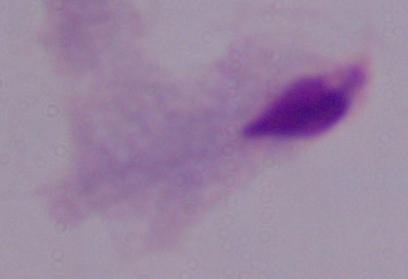

A trichomonad is shown. 1000x magnification. Photomicrograph.